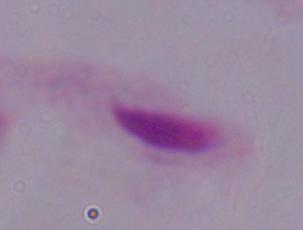 Micrograph. A trichomonad is seen. 1000x magnification.